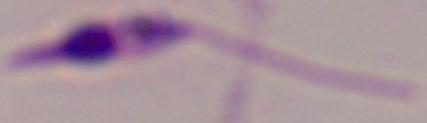
Photomicrograph. A Leishmania parasite is shown. 1000x magnification.